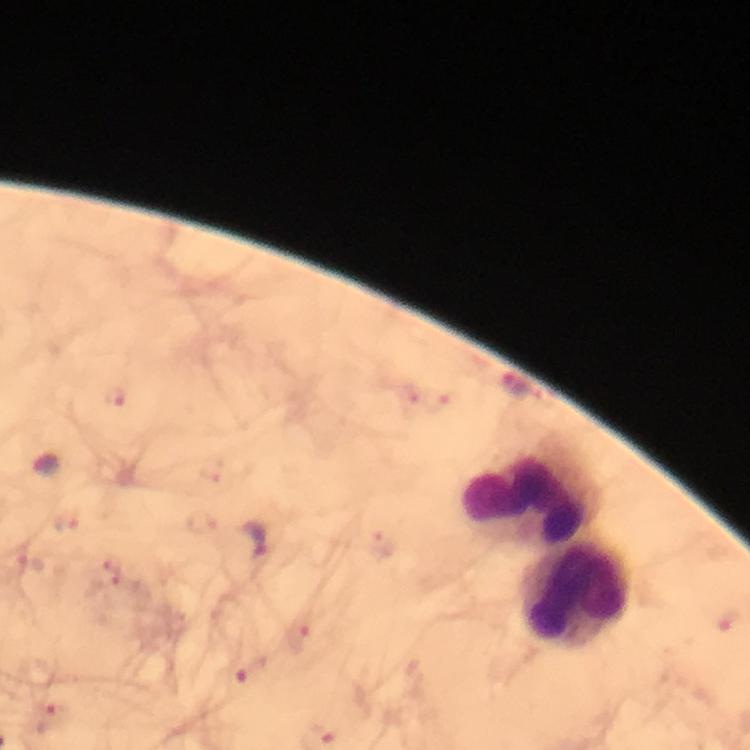
Approximate object centers, in pixels from the top-left corner.
Summary:
  - Malaria parasite locations: (x=116, y=398), (x=437, y=401), (x=211, y=469), (x=201, y=521), (x=66, y=524), (x=254, y=541), (x=383, y=546), (x=106, y=573), (x=727, y=621), (x=299, y=631), (x=251, y=670), (x=54, y=718)
  - Leukocyte locations: (x=525, y=497), (x=575, y=596)
  - Context: from a diagnostic examination for malaria
  - Stain: Giemsa
  - Capture: smartphone camera through the microscope
  - Preparation: thick blood film
  - Cropped from: one field of view
  - Image size: 750×750 pixels
  - Magnification: 100x
  - Immersion oil: applied